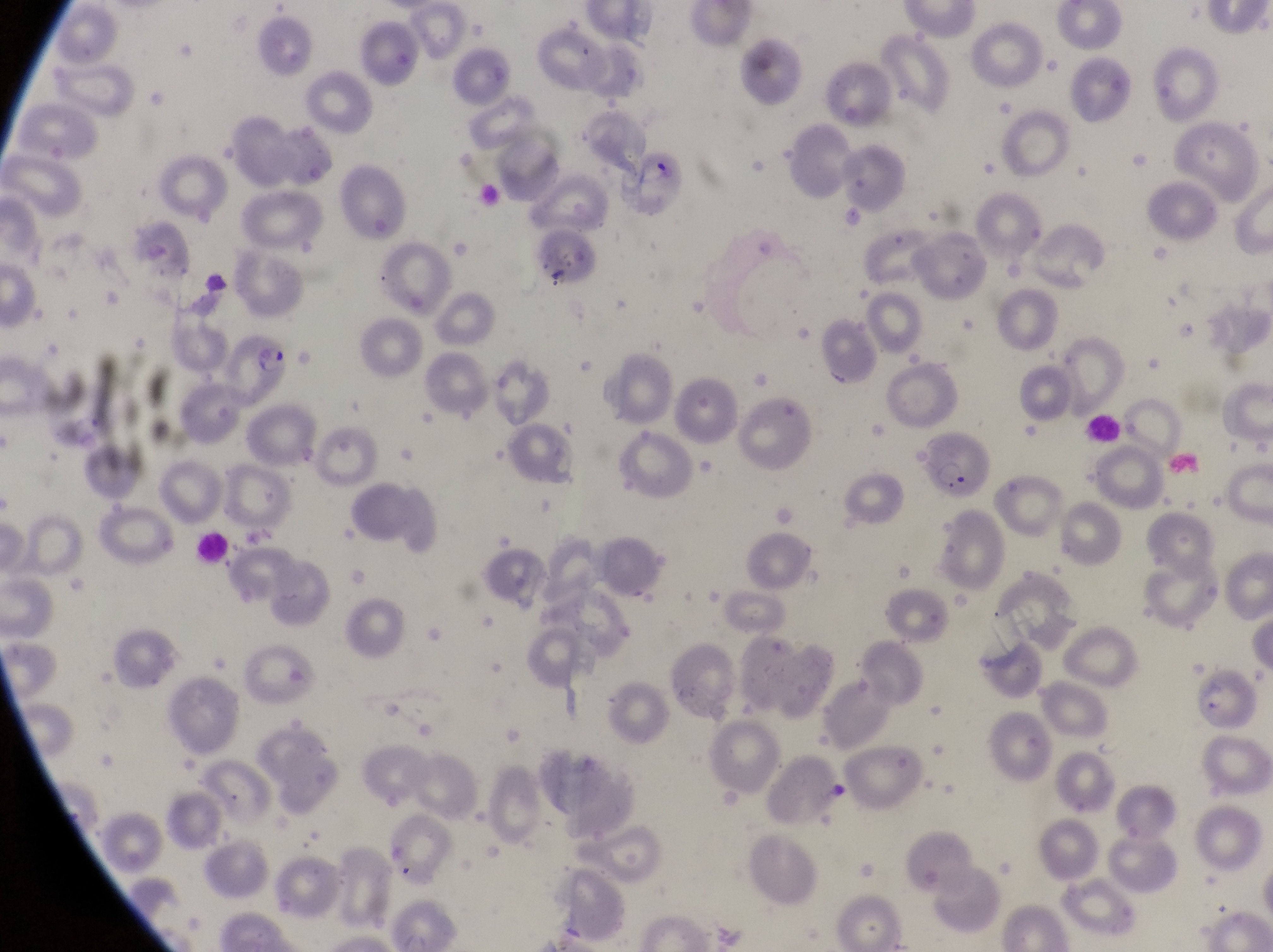 Approximate bounding boxes as left top right bottom in pixels. Leukocyte locations: 1081 412 1126 450; 186 530 234 567. Parasitised red blood cell locations: 625 151 685 206; 532 229 599 294; 217 330 299 408; 916 422 999 507. At a magnification of 1000x. Single field of view. Captured by a smartphone held over the eyepiece of an Olympus CX-23 microscope. Sample from Uganda. Thin blood smear. Image is 1273×952 pixels.